Locate every leukocyte (white blood cell).
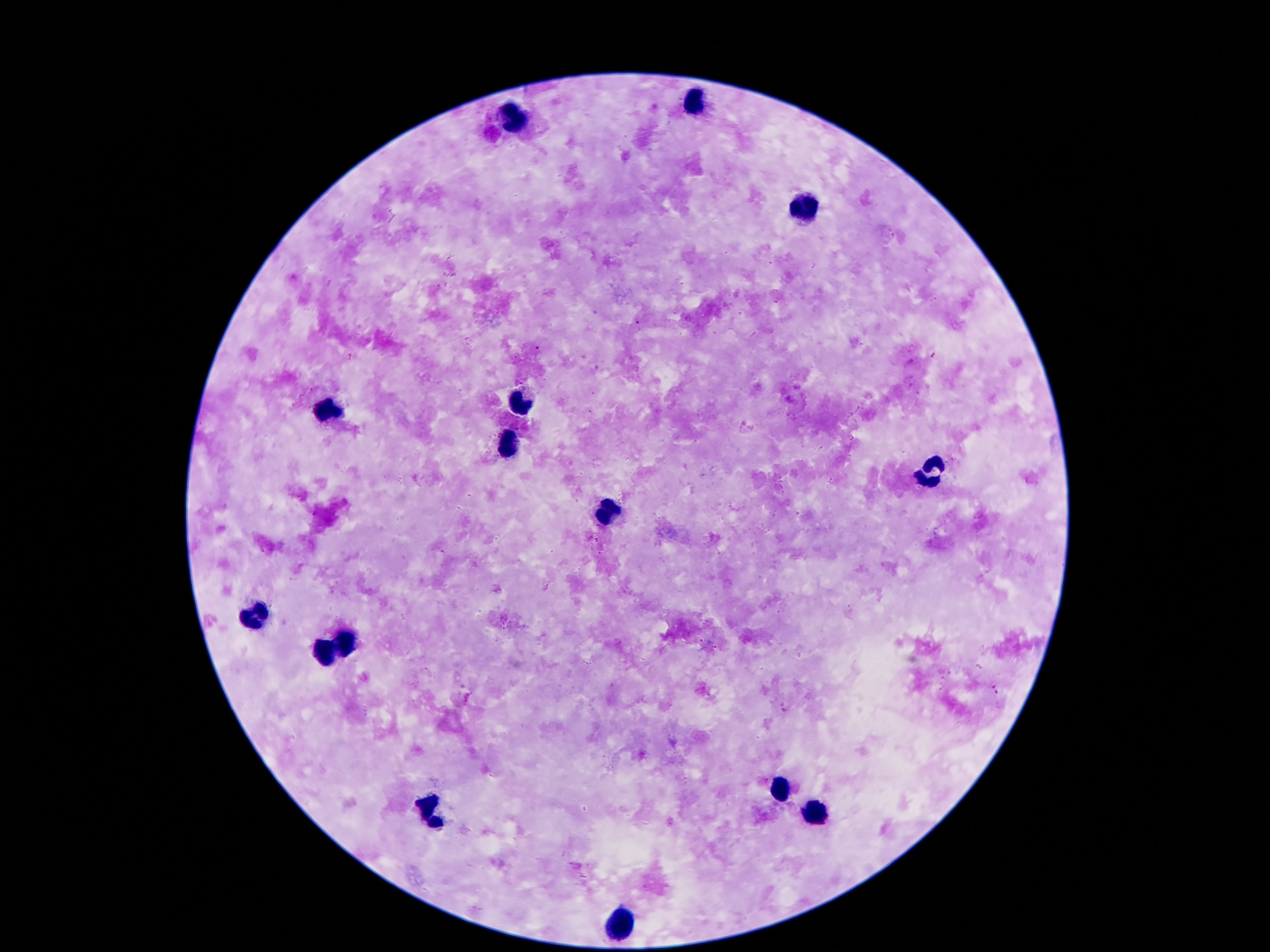

Approximate object centers, in pixels from the top-left corner.
Leukocytes: (x=692, y=102), (x=515, y=119), (x=803, y=209), (x=519, y=400), (x=331, y=408), (x=509, y=443), (x=928, y=472), (x=608, y=511), (x=257, y=615), (x=348, y=643), (x=327, y=650), (x=777, y=790), (x=426, y=810), (x=815, y=812), (x=615, y=926).

Summary:
  - Preparation: thick blood film
  - Magnification: 100x
  - Stain: Giemsa
  - Patient malaria status: uninfected
  - Capture: smartphone camera through the microscope eyepiece
  - Field of view: single
  - Image size: 1270×952 pixels